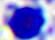

modality = photomicrograph
magnification = 400x
identification = white blood cell